Report the malaria status of this cell.
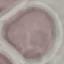
It is uninfected.

image type = automatically extracted cell patch, resized to 64 × 64 pixels
stain = Giemsa
preparation = thin smear
capture = smartphone through the microscope eyepiece